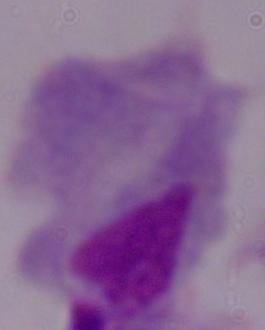

modality = photomicrograph
identification = trichomonad
magnification = 1000x